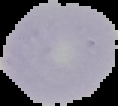 From a thin blood film. Cell region segmented out of the field of view; the surrounding area is masked to black. Image is 118×106 pixels. Result: no malaria parasites detected.